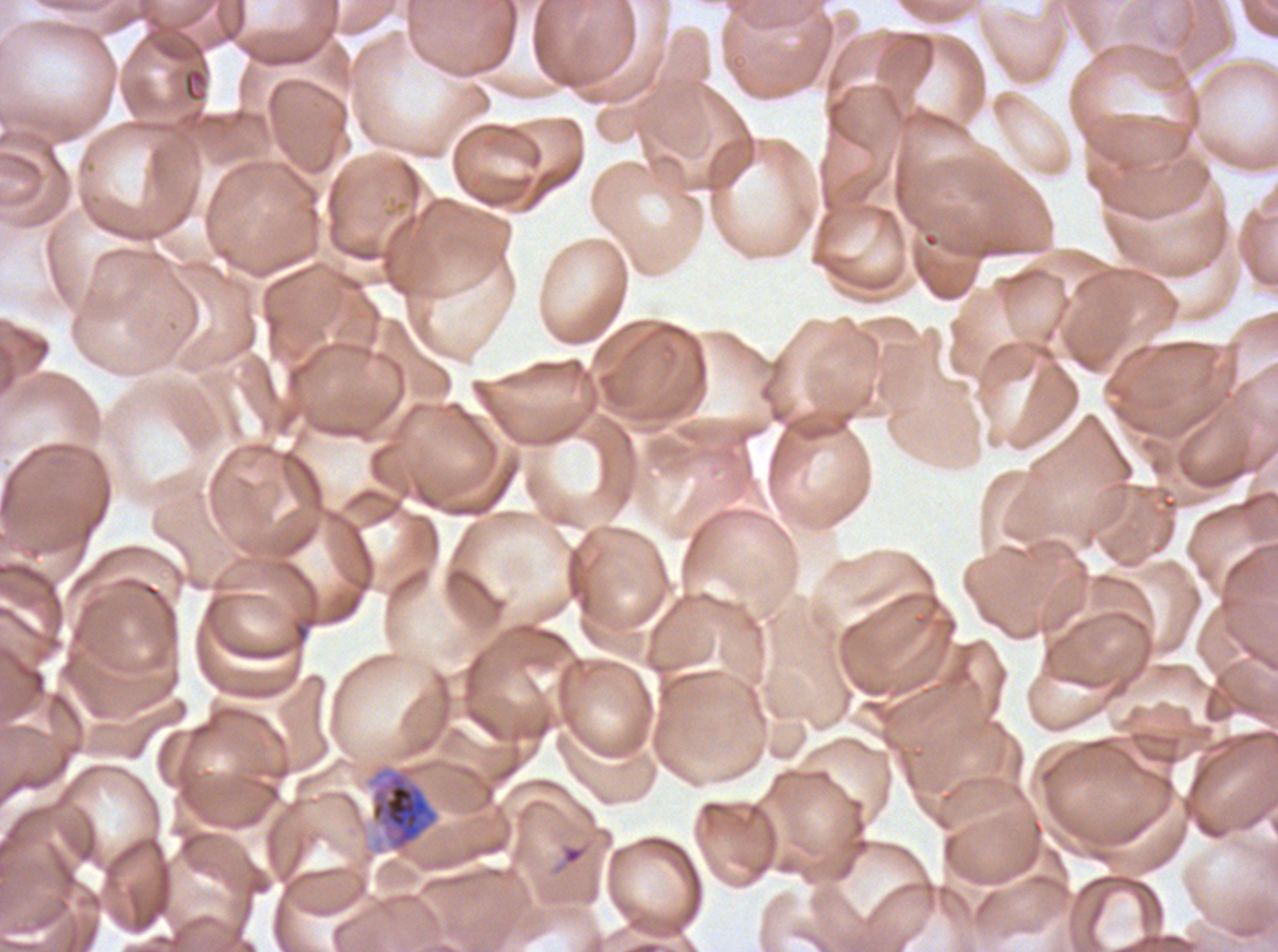
Approximate bounding rectangles given as corner coordinates in pixels from the top-left.
Summary:
  - Late schizont locations: (x1=365, y1=763, x2=440, y2=853)
  - Ring locations: (x1=562, y1=845, x2=585, y2=865)
  - Image size: 1278×952 pixels
  - Stain: Giemsa
  - Field of view: one sub-image of a larger composite
  - Life-cycle stages observed: ring, late schizont
  - Specimen: Plasmodium falciparum from a patient in The Gambia, cultured ex vivo for 24 to 48 hours
  - Preparation: thin blood smear